Comment on the morphology of the erythrocytes.
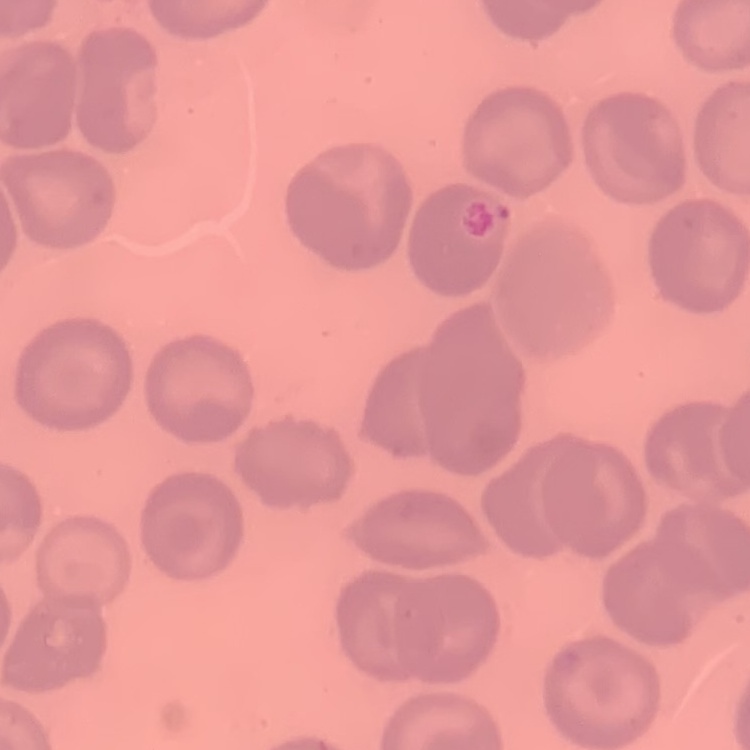

They show no rouleaux formation.

Summary:
  - Preparation: thin peripheral smear
  - Image type: one tile cut from a larger photomicrograph
  - Stain: Field's or Giemsa